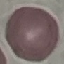
Result: no malaria parasites detected. Thin smear of blood. Giemsa-stained preparation. Automatically extracted cell patch, resized to 64 × 64 pixels. Acquired by smartphone through the microscope eyepiece.